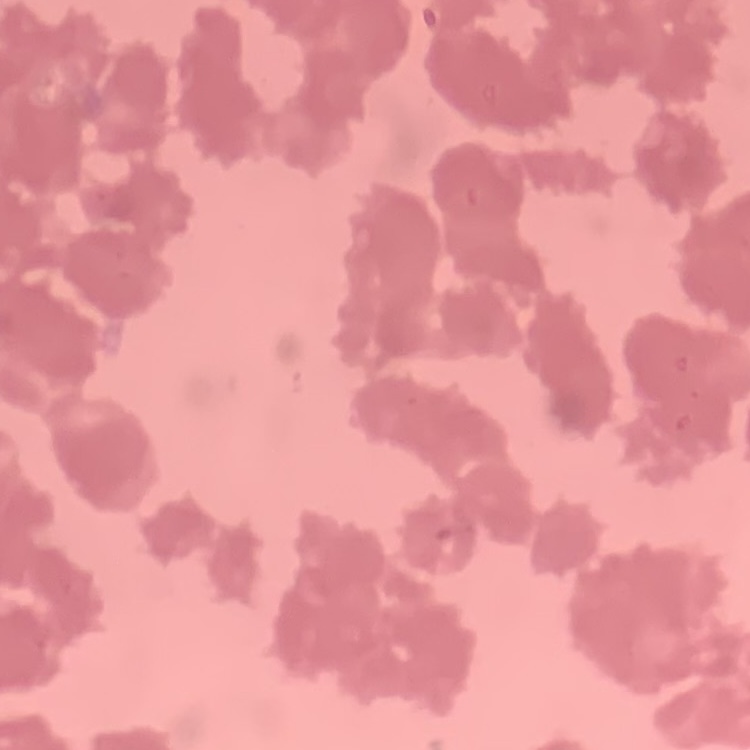
Summary:
  - Red blood cell morphology: rouleaux formation
  - Image type: square crop of a larger photomicrograph
  - Preparation: thin blood smear
  - Stain: Field's or Giemsa